Classify this cell by malaria status.
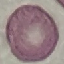

It is uninfected.

{
  "preparation": "thin blood smear",
  "stain": "Giemsa",
  "capture": "smartphone through the microscope eyepiece",
  "image_type": "automatically extracted cell patch, resized to 64 × 64 pixels"
}